Report the malaria status of this cell.
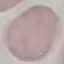

It is uninfected.

image_type: automatically extracted cell patch, resized to 64 × 64 pixels
stain: Giemsa
capture: smartphone through the microscope eyepiece
preparation: thin smear